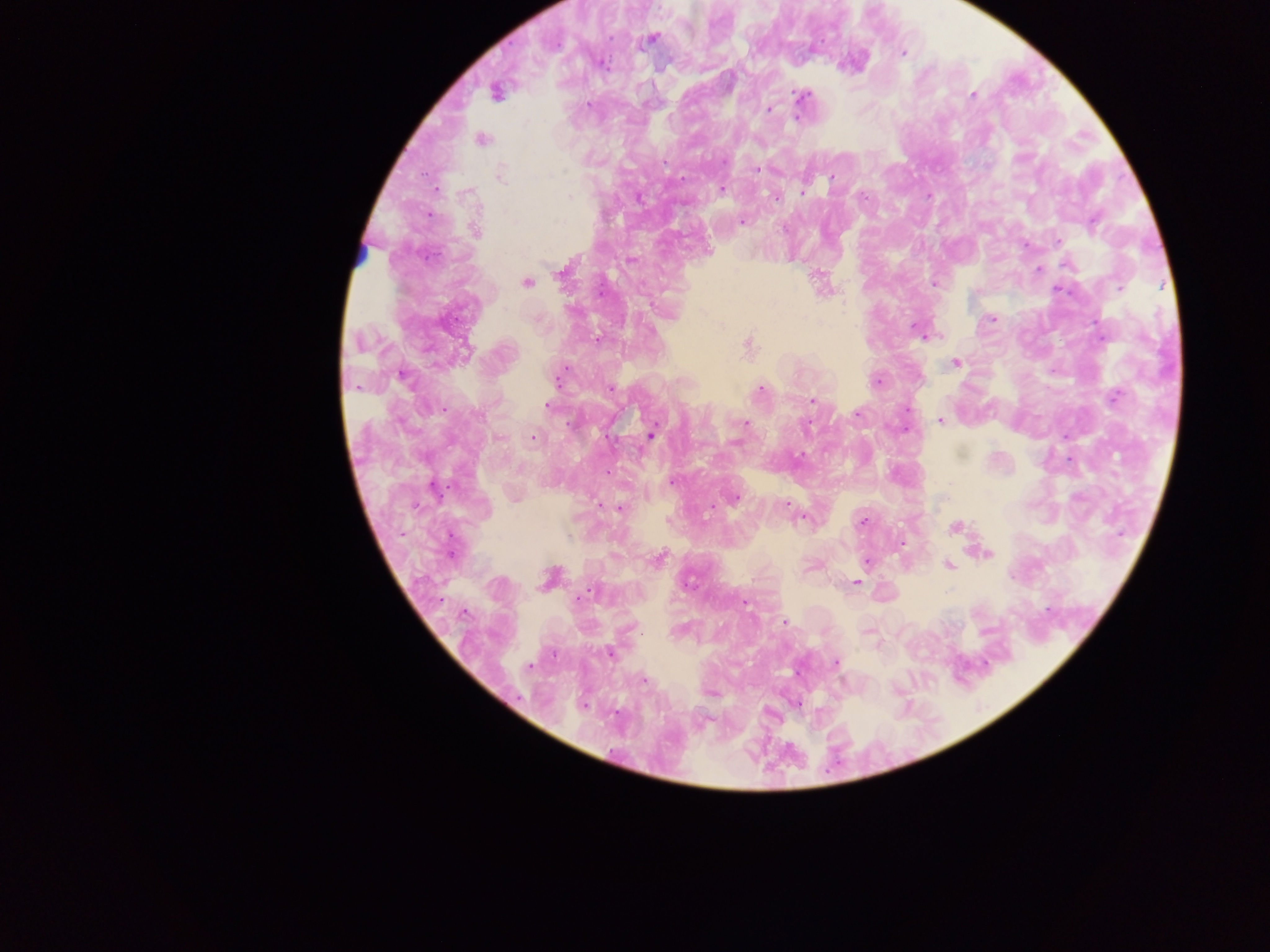
capture: mobile-phone photograph through a microscope
image_size: 1270×952 pixels
field_of_view: single
malaria_parasite_locations: 'approximate centers as {x, y} in pixels: {651, 39}, {902, 53}, {602, 63}, {496, 92}, {802, 95}, {972, 95}, {589, 104}, {770, 110}, {482, 140}, {755, 170}, {502, 175}, {832, 177}, {721, 189}, {803, 190}, {570, 197}, {776, 199}, {742, 222}, {1093, 223}, {783, 229}, {475, 230}, {1058, 240}, {1068, 265}, {1039, 269}, {562, 271}, {527, 283}, {935, 283}, {992, 318}, {919, 331}, {749, 344}, {466, 351}, {956, 363}, {402, 375}, {558, 378}, {877, 381}, {610, 389}, {761, 389}, {1115, 397}, {812, 401}, {548, 406}, {858, 414}, {478, 415}, {940, 421}, {746, 423}, {806, 426}, {651, 435}, {533, 437}, {735, 444}, {671, 481}, {435, 490}, {735, 498}, {787, 507}, {617, 508}, {862, 522}, {955, 527}, {988, 554}, {658, 559}, {867, 561}, {948, 565}, {547, 578}, {856, 582}, {688, 583}, {586, 594}, {462, 613}, {784, 621}, {609, 653}, {836, 662}, {529, 666}, {643, 681}, {584, 705}'
preparation: thick blood smear
country: Ghana